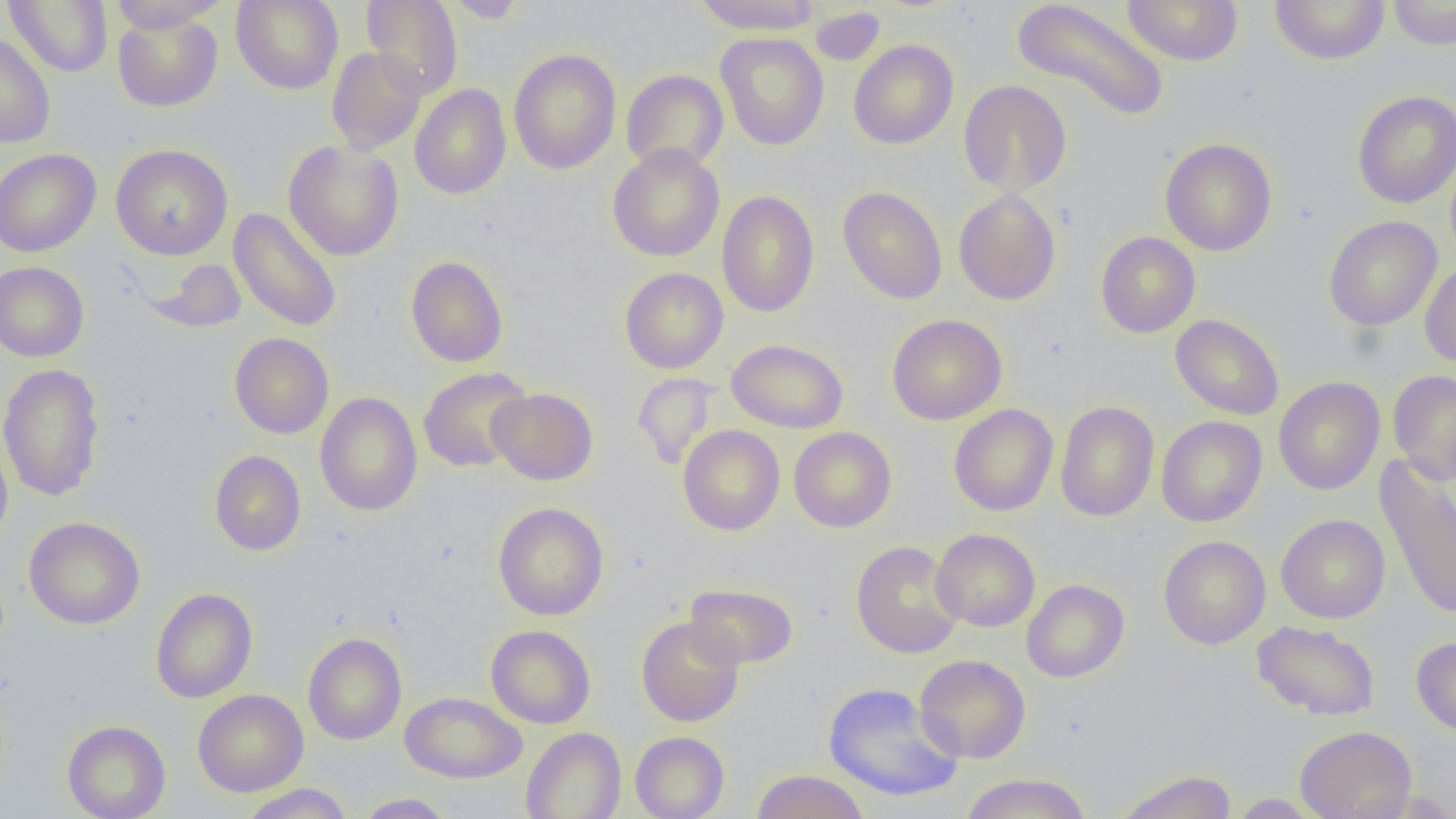 Approximate bounding boxes as (x1, y1, x2, y2) in pixels. Uninfected red blood cell locations: (5, 0, 113, 77), (231, 0, 344, 94), (361, 0, 463, 99), (444, 0, 529, 23), (692, 0, 823, 34), (1012, 0, 1170, 122), (1121, 0, 1244, 66), (1269, 0, 1390, 65), (1387, 0, 1456, 50), (108, 1, 226, 33), (811, 7, 885, 65), (113, 10, 223, 112), (0, 31, 56, 148), (716, 32, 829, 150), (848, 39, 958, 150), (327, 47, 427, 154), (508, 48, 621, 175), (620, 69, 729, 174), (958, 80, 1072, 196), (409, 84, 511, 200), (1352, 90, 1456, 208), (1159, 137, 1277, 256), (283, 140, 404, 261), (608, 143, 725, 262), (111, 144, 233, 260), (0, 148, 101, 257), (838, 186, 947, 304), (953, 188, 1061, 305), (716, 190, 820, 317), (229, 209, 342, 332), (1323, 215, 1442, 331), (1095, 232, 1200, 338), (406, 256, 508, 367), (145, 258, 248, 333), (1419, 261, 1456, 369), (0, 262, 89, 362), (619, 267, 728, 374), (887, 313, 1007, 425), (1170, 314, 1284, 420), (230, 333, 334, 438), (727, 339, 849, 433), (0, 362, 106, 502), (418, 367, 533, 473), (1388, 369, 1456, 485), (632, 373, 720, 471), (1273, 376, 1385, 495), (487, 387, 598, 485), (314, 392, 423, 516), (1055, 401, 1159, 522), (948, 404, 1059, 517), (1156, 416, 1267, 527), (678, 425, 785, 535), (788, 427, 897, 532), (0, 434, 13, 548), (210, 450, 305, 556), (1375, 457, 1456, 620), (492, 502, 609, 620), (1276, 514, 1390, 623), (24, 517, 145, 629), (930, 528, 1040, 632), (1158, 535, 1271, 648), (850, 540, 964, 658), (1021, 579, 1129, 682), (684, 583, 798, 670), (150, 587, 257, 703), (636, 616, 745, 727), (1251, 620, 1381, 721), (486, 624, 596, 728), (303, 632, 407, 745), (1411, 636, 1456, 737), (914, 654, 1031, 763), (823, 682, 964, 803), (193, 689, 308, 796), (400, 692, 526, 783), (62, 720, 171, 819), (1295, 725, 1416, 818), (521, 727, 626, 819), (630, 731, 729, 819), (751, 769, 870, 819), (1113, 770, 1238, 819), (959, 773, 1092, 819), (239, 784, 353, 818), (354, 793, 455, 818), (1228, 793, 1324, 818). Slide-level diagnosis: negative for blood parasites. Image is 1456×819 pixels. Captured at 1000x magnification. Thin blood film. Light microscopy. Single field of view.